Classify this cell by malaria status.
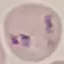
It is parasitized.

Summary:
  - Image type: cell patch, automatically extracted from a larger field of view and resized to 64 × 64 pixels
  - Stain: Giemsa
  - Capture: smartphone through the microscope eyepiece
  - Preparation: thin blood film